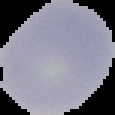 Result: malaria parasites detected. From a thin blood film. Image is 115×115 pixels. Segmented cell region on a black background.